Locate every malaria parasite.
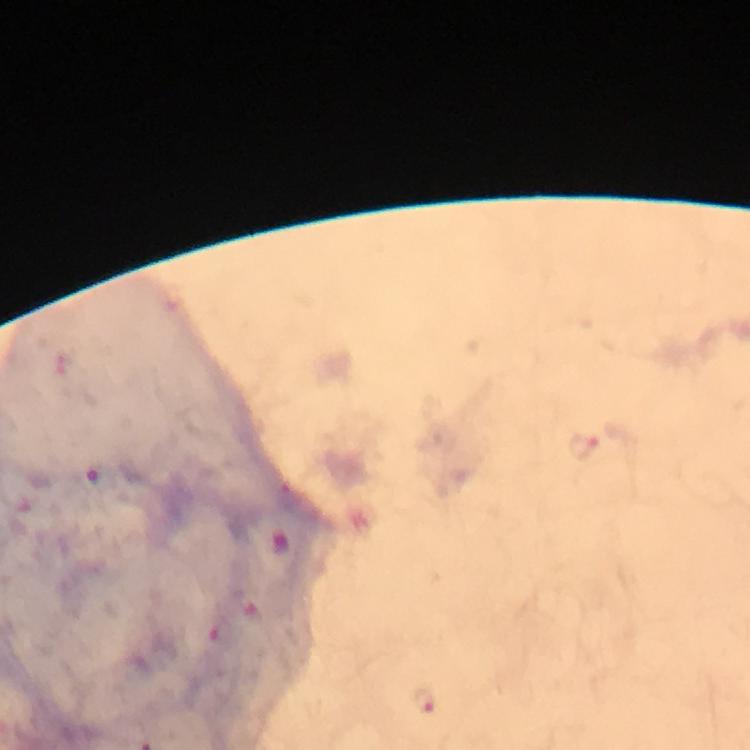

Approximate object centers, in pixels from the top-left corner.
Malaria parasites: (x=582, y=446), (x=426, y=697).

Summary:
  - Preparation: thick blood film
  - Image size: 750×750 pixels
  - Immersion oil: used
  - Capture: smartphone photograph through a microscope
  - Context: from a malaria diagnostic workup
  - Stain: Giemsa
  - Magnification: 100x
  - Cropped from: a single field of view